Point out every malaria parasite and every leukocyte.
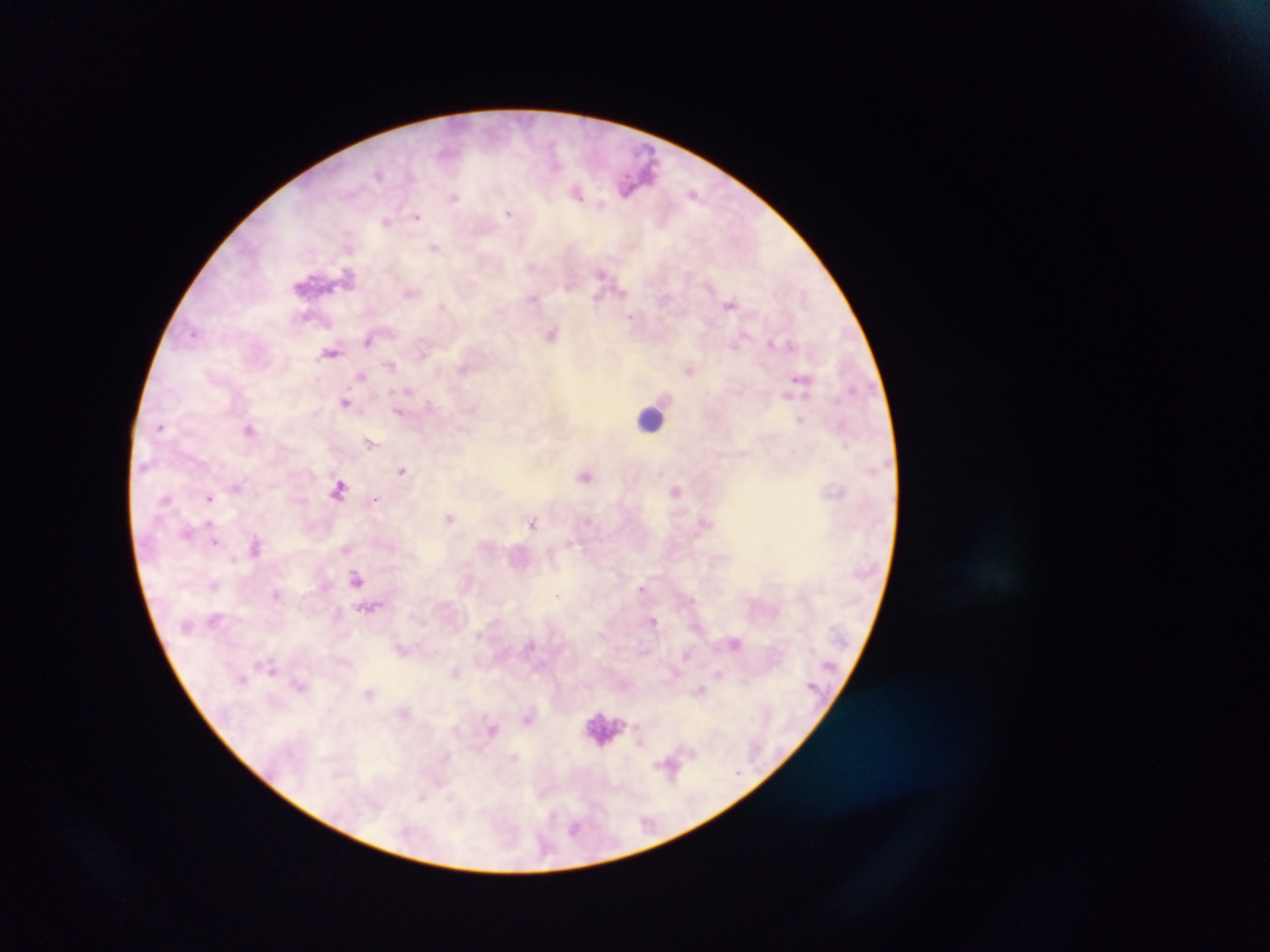

Approximate centers as [x, y] in pixels.
Malaria parasites: [379, 174], [693, 192], [577, 193], [454, 196], [508, 213], [417, 217], [387, 221], [435, 247], [348, 273], [601, 273], [623, 292], [410, 293], [533, 298], [597, 301], [730, 305], [630, 317], [193, 333], [552, 334], [368, 341], [770, 343], [734, 344], [791, 345], [330, 352], [423, 354], [390, 366], [463, 369], [690, 370], [361, 375], [800, 377], [408, 390], [786, 394], [345, 402], [429, 404], [398, 411], [800, 420], [160, 426], [249, 430], [370, 443], [402, 470], [585, 476], [237, 487], [339, 488], [675, 490], [209, 498], [166, 499], [375, 499], [450, 518], [533, 522], [210, 523], [187, 532], [215, 542], [570, 544], [255, 546], [346, 549], [234, 558], [357, 578], [214, 585], [642, 588], [275, 593], [556, 595], [653, 621], [736, 643], [687, 654], [272, 670], [456, 671], [719, 674], [243, 679], [300, 686], [701, 690], [369, 693], [527, 716], [493, 728], [515, 756], [670, 767], [422, 797], [574, 829].
Leukocytes: [651, 419], [600, 725].

preparation = thick blood film
capture = mobile-phone photograph through a microscope
field of view = single
country = Ghana
image size = 1270×952 pixels